Describe the morphology of the red blood cells.
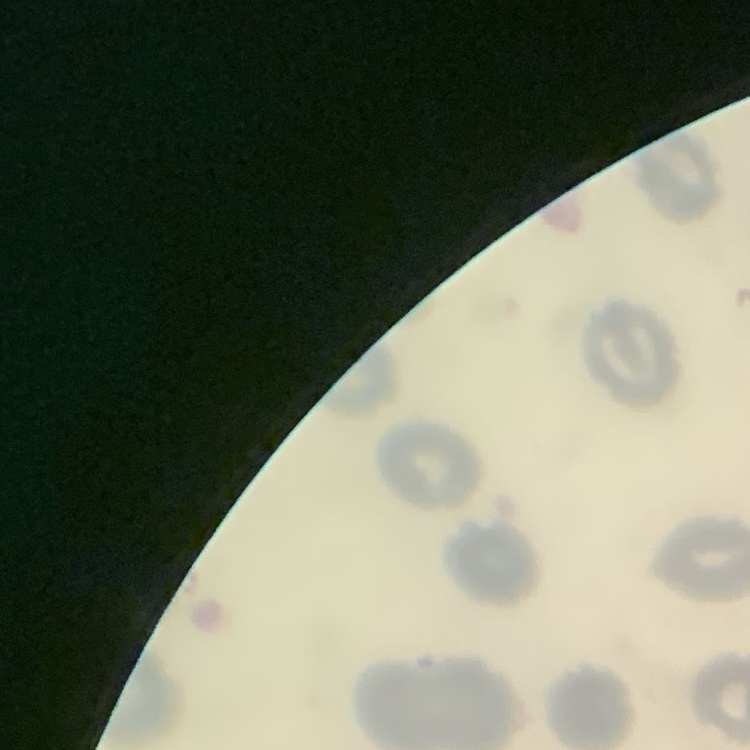
No rouleaux formation.

Summary:
  - Preparation: thin blood smear
  - Image type: one tile cut from a larger photomicrograph
  - Stain: Field's or Giemsa